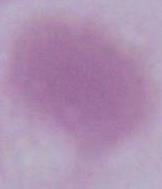
modality = photomicrograph
magnification = 1000x
identification = red blood cell